Locate leukocytes (white blood cells).
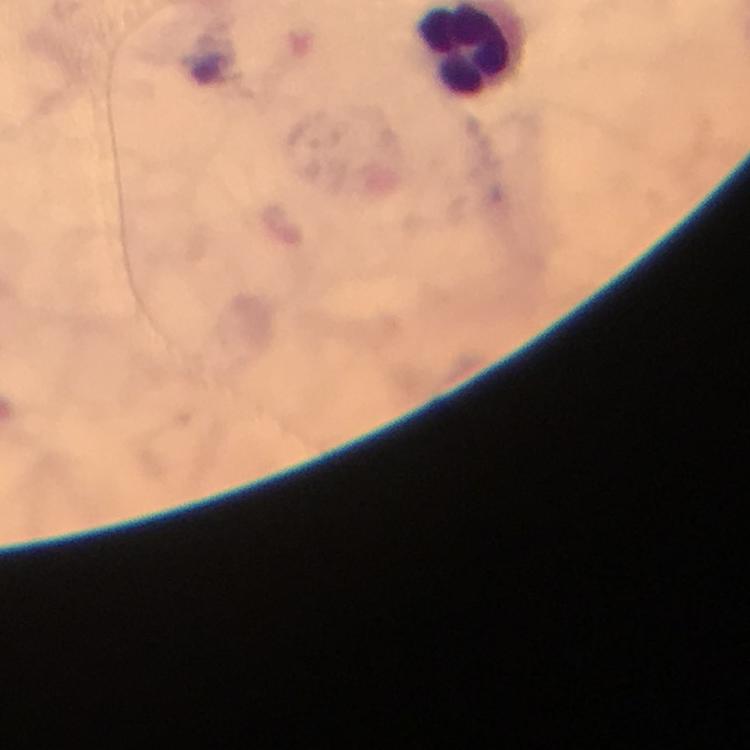

Approximate centers as (x, y) in pixels.
Leukocytes: (466, 50).

magnification = 100x
context = from a malaria diagnostic workup
preparation = thick smear
capture = smartphone photograph through a microscope
immersion oil = applied
image size = 750×750 pixels
malaria parasites = none seen
stain = Giemsa
cropped from = one field of view